State the preparation type.
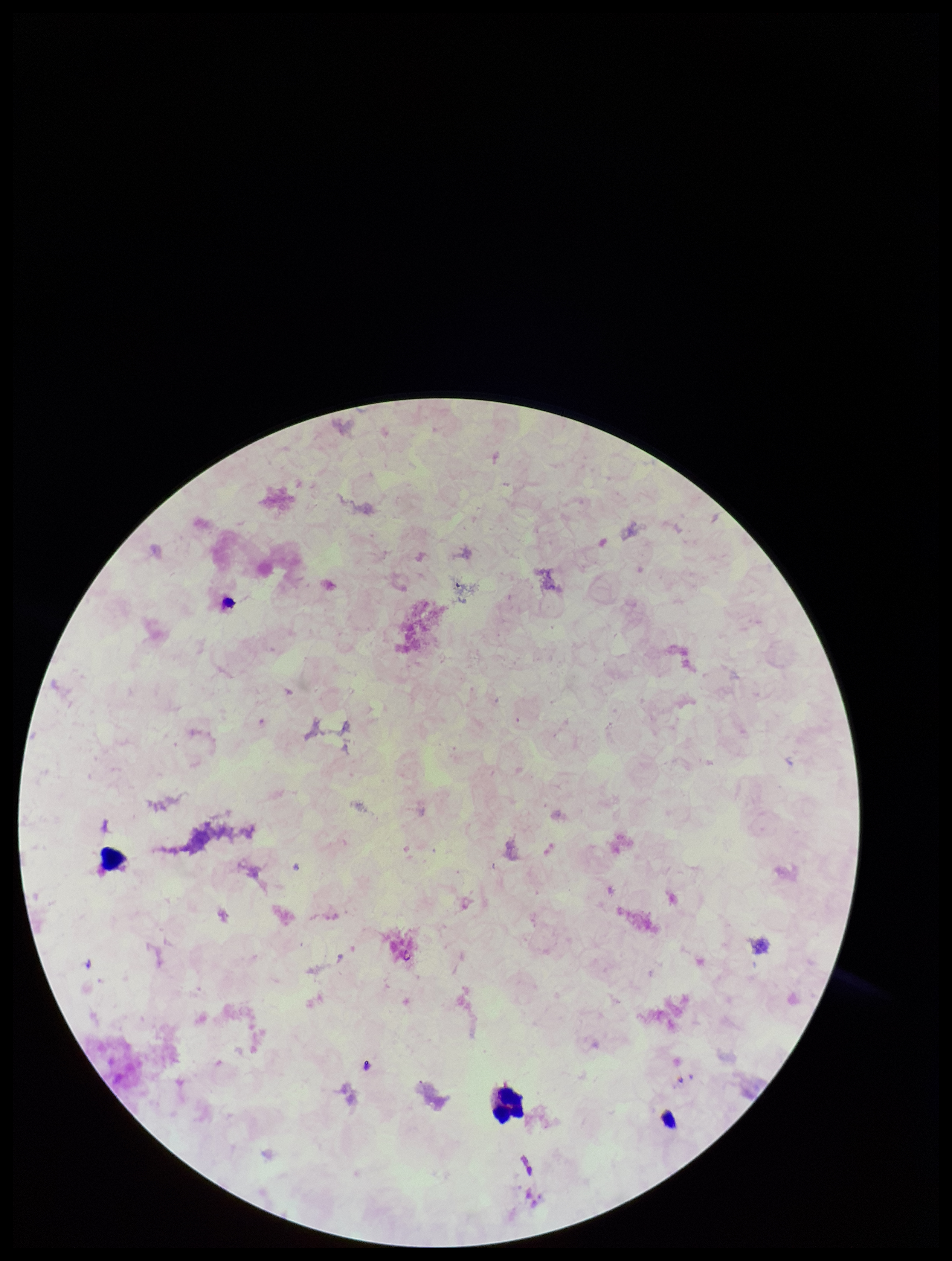
It is a thick blood smear.

Summary:
  - Leukocyte count: 2
  - Parasite count: 0
  - Capture: smartphone photograph through the microscope eyepiece
  - Image size: 952×1261 pixels
  - Stain: Giemsa
  - Field of view: single
  - Patient malaria status: negative
  - Plasmodium parasites: none seen